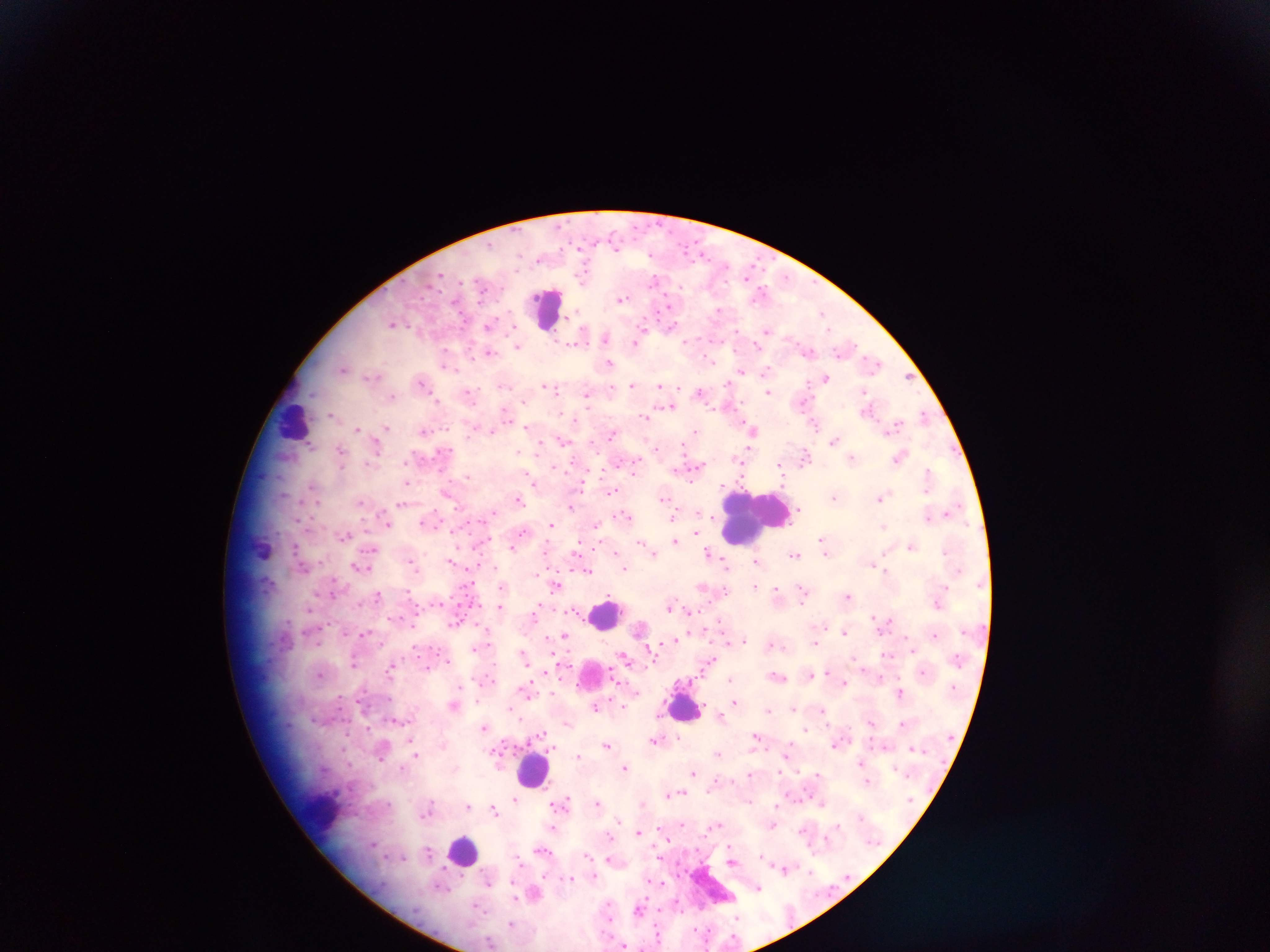

Approximate centers as [x, y] in pixels. Leukocyte locations: [547, 309], [294, 420], [753, 517], [604, 614], [592, 674], [685, 706], [534, 769], [323, 811], [463, 849]. Plasmodium parasite locations: [615, 246], [539, 260], [583, 275], [440, 276], [655, 279], [482, 289], [761, 293], [621, 299], [666, 306], [719, 309], [823, 313], [392, 323], [488, 326], [671, 327], [513, 329], [828, 329], [767, 330], [737, 331], [606, 339], [635, 342], [688, 342], [758, 345], [517, 347], [489, 353], [710, 361], [610, 363], [874, 363], [343, 368], [767, 370], [742, 372], [371, 375], [908, 377], [825, 378], [421, 382], [728, 384], [632, 385], [505, 386], [660, 386], [553, 388], [612, 388], [769, 391], [469, 392], [700, 392], [864, 392], [587, 395], [391, 396], [437, 400], [671, 406], [866, 409], [505, 412], [331, 414], [924, 415], [644, 416], [815, 425], [895, 425], [386, 426], [527, 427], [357, 429], [752, 430], [423, 431], [492, 431], [695, 432], [611, 435], [563, 441], [834, 441], [311, 444], [340, 449], [377, 449], [444, 452], [519, 452], [804, 457], [852, 457], [899, 457], [634, 465], [556, 467], [696, 467], [782, 473], [928, 473], [468, 476], [530, 479], [406, 482], [581, 483], [311, 487], [610, 492], [448, 495], [834, 497], [882, 497], [664, 498], [518, 499], [360, 503], [401, 503], [570, 507], [799, 510], [952, 510], [492, 514], [625, 515], [673, 517], [424, 522], [387, 523], [551, 525], [883, 526], [597, 527], [522, 532], [696, 533], [344, 536], [822, 539], [675, 541], [641, 543], [911, 546], [512, 547], [577, 547], [824, 547], [370, 550], [616, 552], [944, 552], [708, 553], [654, 554], [795, 555], [452, 560], [755, 561], [411, 562], [726, 564], [875, 564], [358, 567], [624, 568], [883, 568], [588, 570], [556, 585], [755, 585], [701, 588], [776, 589], [410, 593], [803, 594], [378, 595], [848, 595], [499, 605], [670, 605], [309, 609], [536, 610], [687, 610], [873, 615], [455, 623], [844, 632], [365, 633], [935, 635], [564, 636], [676, 640], [744, 640], [815, 642], [774, 645], [475, 648], [912, 650], [888, 654], [524, 656], [625, 658], [709, 661], [354, 662], [390, 669], [427, 669], [828, 671], [923, 672], [320, 674], [811, 675], [778, 676], [729, 679], [844, 682], [527, 689], [635, 692], [900, 693], [734, 702], [453, 705], [595, 706], [794, 707], [769, 710], [823, 711], [721, 715], [871, 722], [568, 724], [903, 724], [484, 728], [806, 730], [756, 736], [654, 740], [412, 743], [606, 744], [835, 745], [913, 748], [788, 749], [381, 754], [414, 754], [717, 754], [578, 755], [861, 763], [626, 768], [693, 772], [749, 774], [817, 774], [867, 780], [674, 794], [515, 799], [563, 802], [597, 803], [642, 804], [468, 806], [428, 807], [493, 809], [618, 820], [718, 825], [772, 826], [837, 826], [553, 829], [802, 831], [638, 832], [608, 837], [542, 851], [428, 852], [761, 855], [587, 856], [519, 858], [609, 859], [785, 870], [810, 871], [594, 876], [571, 878], [489, 880], [758, 887], [534, 892], [638, 909], [737, 917], [511, 923], [491, 942], [626, 946]. Single field of view. Photographed through a microscope with a mobile-phone camera. Collected in Ghana. Image is 1270×952 pixels. Thick blood smear.